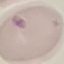 Malaria status: uninfected. Acquired by smartphone through the microscope eyepiece. Giemsa stain. Cell patch, automatically extracted from a larger field of view and resized to 64 × 64 pixels. Thin smear of blood.